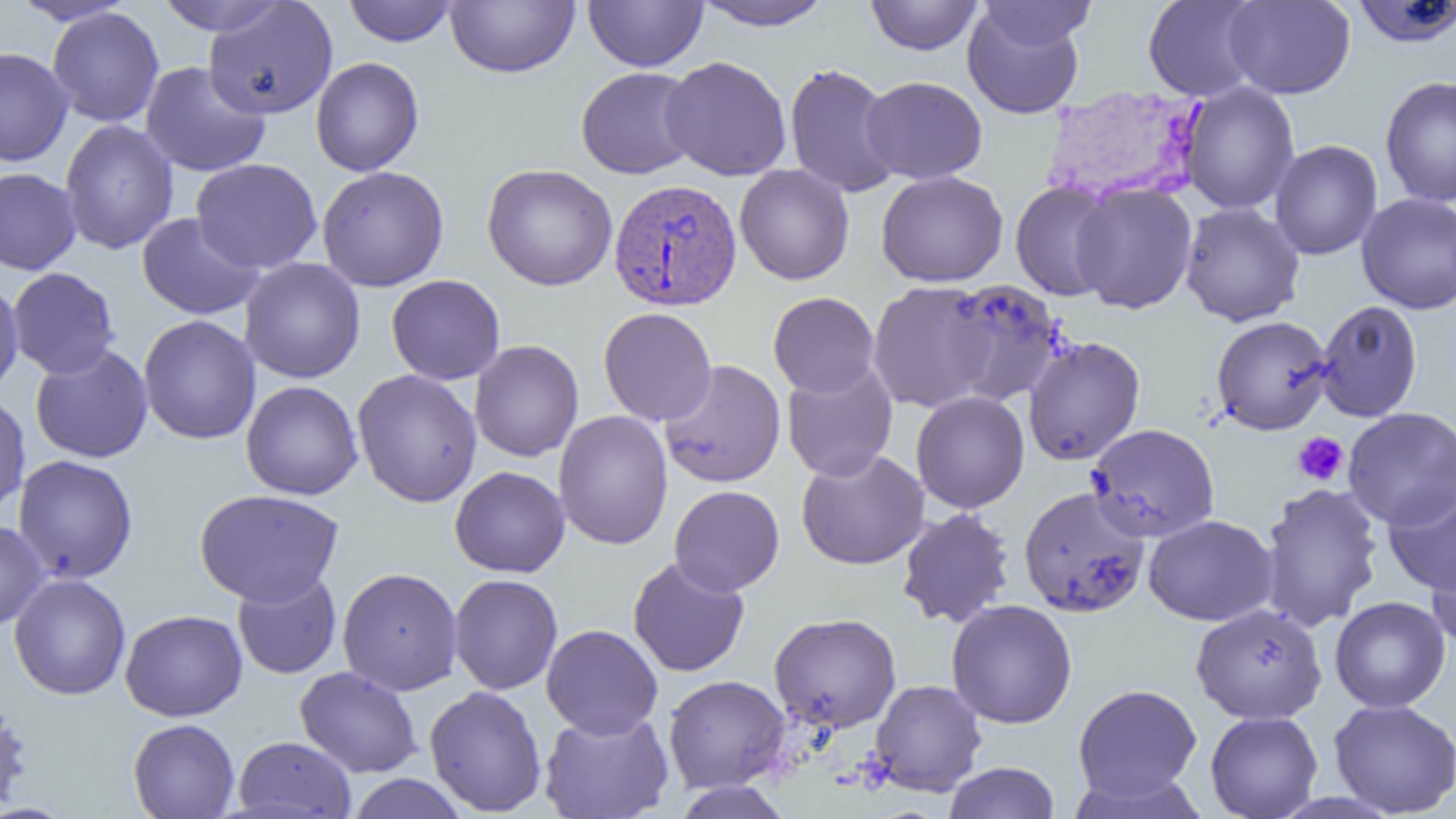

Approximate bounding boxes as [x1, y1, x2, y2] in pixels. Plasmodium vivax-infected red blood cell locations: [1036, 78, 1207, 199], [608, 178, 743, 311]. Uninfected red blood cell locations: [8, 0, 138, 26], [153, 0, 291, 36], [445, 0, 580, 78], [583, 0, 708, 72], [866, 0, 983, 56], [975, 0, 1097, 52], [1142, 0, 1266, 102], [1223, 0, 1356, 99], [343, 1, 458, 46], [690, 1, 836, 31], [1351, 1, 1456, 48], [203, 2, 338, 119], [962, 3, 1087, 119], [47, 7, 164, 127], [0, 47, 74, 167], [660, 56, 793, 181], [311, 57, 424, 176], [140, 61, 270, 177], [785, 63, 901, 198], [575, 67, 701, 179], [1380, 74, 1456, 208], [860, 76, 988, 184], [1180, 82, 1300, 214], [59, 119, 179, 255], [1269, 139, 1383, 260], [191, 158, 322, 273], [482, 163, 617, 291], [735, 164, 855, 285], [317, 165, 449, 291], [0, 168, 82, 275], [876, 170, 1008, 287], [1010, 180, 1120, 301], [1071, 183, 1198, 314], [1356, 193, 1456, 314], [1180, 202, 1305, 326], [137, 213, 265, 319], [240, 257, 366, 384], [7, 267, 120, 379], [386, 274, 505, 385], [0, 278, 24, 397], [942, 279, 1068, 407], [867, 280, 998, 412], [768, 292, 880, 398], [1315, 300, 1422, 422], [598, 307, 717, 426], [138, 315, 261, 445], [1211, 316, 1333, 435], [1023, 336, 1146, 466], [469, 340, 584, 462], [30, 344, 154, 463], [659, 359, 786, 488], [782, 362, 898, 481], [352, 370, 483, 508], [241, 380, 363, 499], [911, 391, 1030, 513], [0, 392, 31, 516], [1342, 406, 1456, 529], [553, 410, 672, 550], [1086, 423, 1219, 543], [796, 449, 929, 570], [13, 454, 138, 583], [449, 466, 570, 578], [1258, 482, 1384, 631], [1383, 482, 1456, 595], [669, 485, 785, 596], [1018, 486, 1151, 618], [194, 489, 344, 606], [896, 507, 1015, 628], [1144, 514, 1277, 625], [0, 519, 49, 631], [1428, 542, 1456, 652], [628, 558, 749, 677], [337, 567, 463, 695], [232, 570, 342, 679], [9, 573, 131, 700], [449, 574, 562, 695], [1330, 596, 1451, 713], [946, 599, 1077, 729], [1191, 602, 1327, 723], [120, 609, 247, 721], [769, 612, 902, 732], [541, 624, 663, 739], [295, 666, 423, 778], [663, 674, 790, 792], [870, 679, 987, 797], [1073, 683, 1202, 805], [424, 685, 547, 816], [0, 696, 33, 816], [1329, 699, 1456, 817], [539, 710, 675, 819], [1205, 711, 1323, 819], [128, 718, 240, 818], [232, 735, 357, 818], [943, 762, 1060, 818], [346, 774, 469, 819], [670, 780, 793, 819]. Platelet locations: [1292, 432, 1349, 486]. Slide-level diagnosis: Plasmodium vivax. Light microscopy. 1000x magnification. One field of a larger specimen. Thin blood film. Image is 1456×819 pixels.